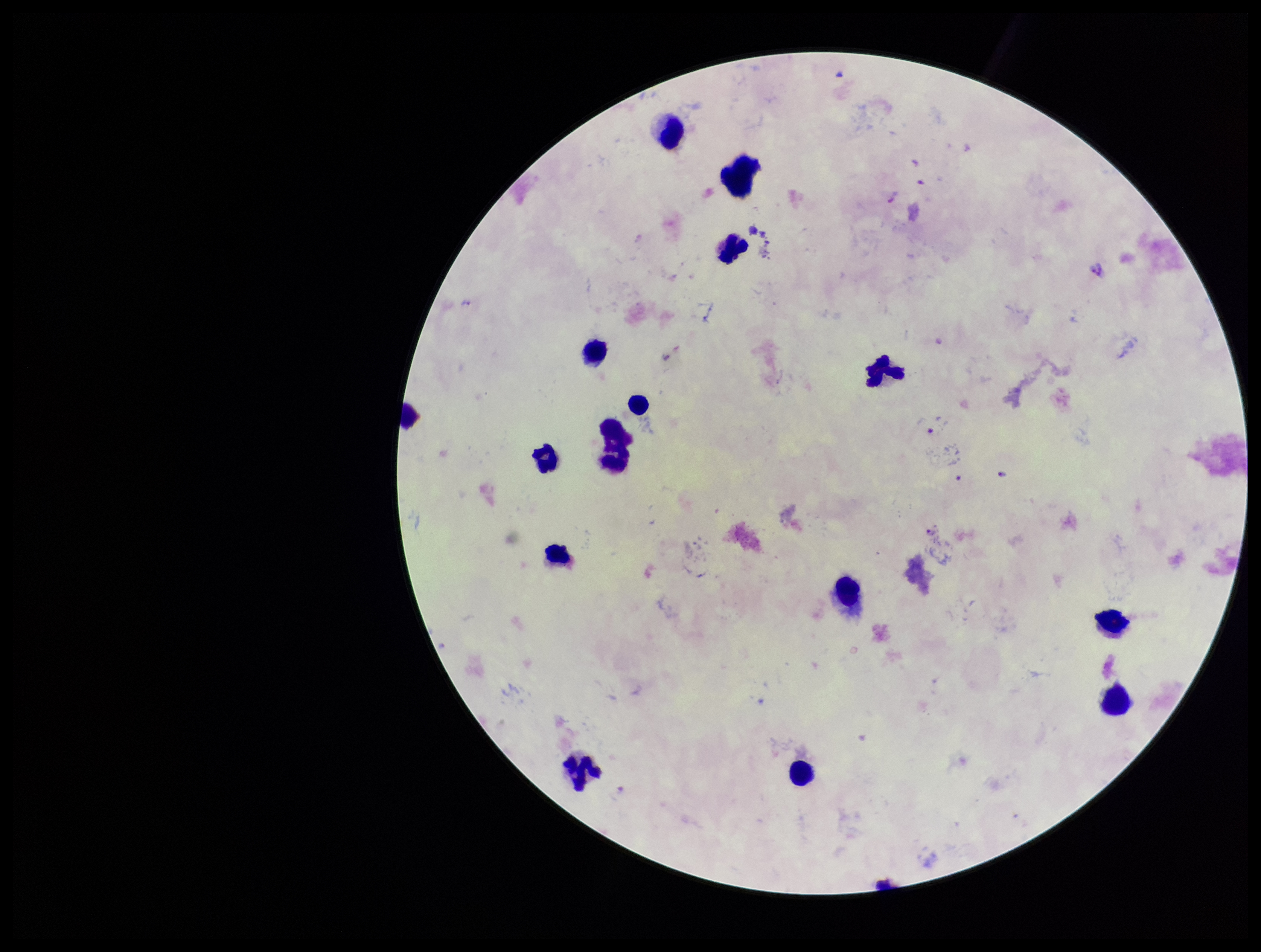
image size = 1261×952 pixels
leukocyte count = 15
species reported for this patient = Plasmodium falciparum
stain = Giemsa
Plasmodium parasites = seen
parasite count = 4
field of view = single
capture = smartphone photograph through the microscope eyepiece
patient malaria status = positive
preparation = thick blood smear